Report the malaria status of this cell.
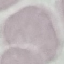
It is uninfected.

{
  "image_type": "automatically extracted cell patch, resized to 64 × 64 pixels",
  "capture": "smartphone through the microscope eyepiece",
  "preparation": "thin blood film",
  "stain": "Giemsa"
}